Assess this cell for malaria.
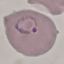
Parasitized.

Summary:
  - Preparation: thin smear
  - Capture: smartphone camera at the microscope eyepiece
  - Image type: cell patch, automatically extracted from a larger field of view and resized to 64 × 64 pixels
  - Stain: Giemsa